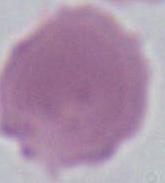
Summary:
  - Magnification: 1000x
  - Modality: photomicrograph
  - Identification: erythrocyte